Point out each Plasmodium parasite.
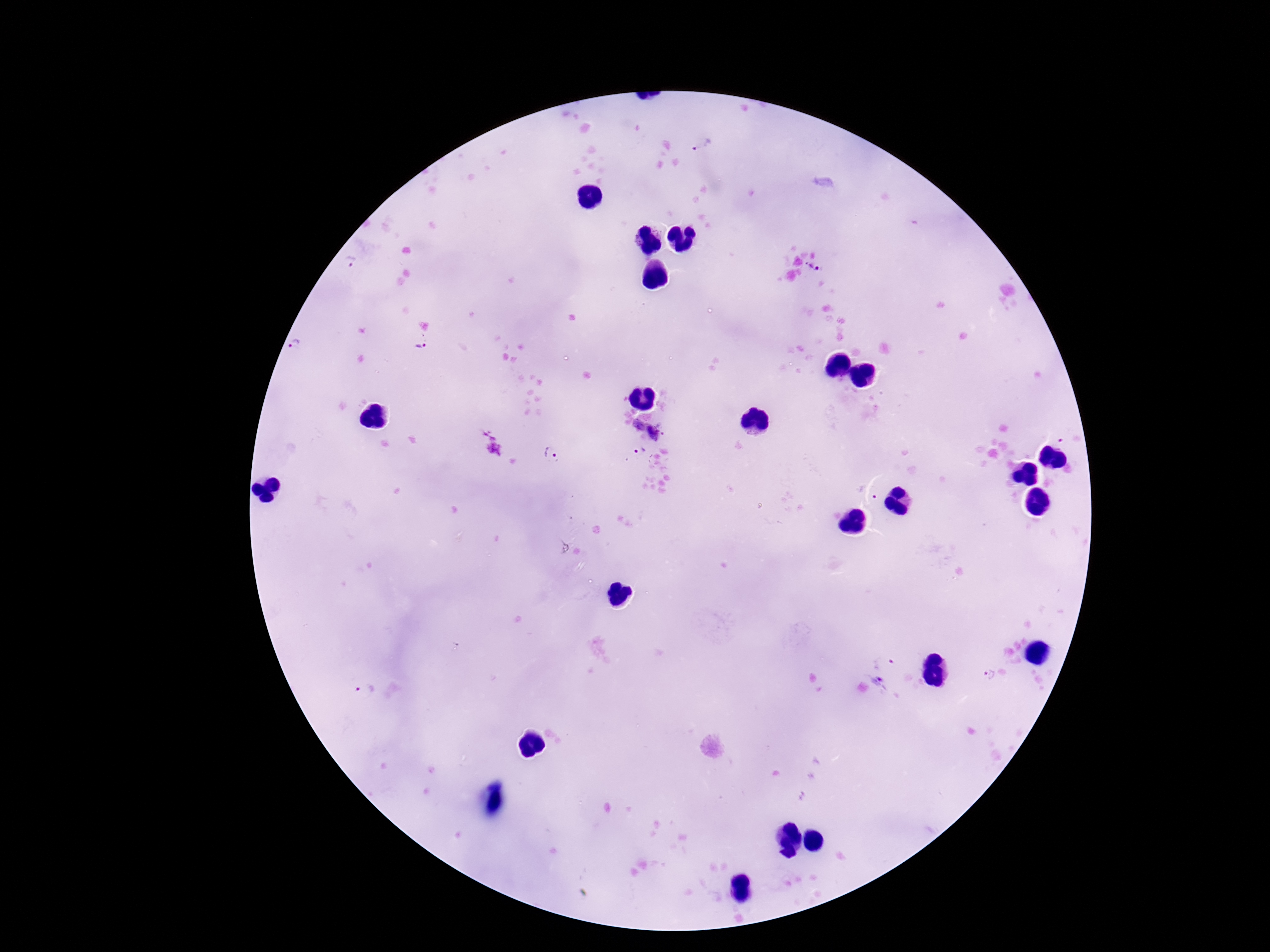
Approximate centers as [x, y] in pixels.
Plasmodium parasites: [703, 145], [350, 261], [809, 266], [817, 269], [296, 345], [419, 345], [637, 425], [655, 434], [1060, 444], [641, 452], [551, 455], [883, 658], [986, 674], [880, 679], [365, 689].

Photographed through the microscope eyepiece with a smartphone camera. 100x magnification. Thick blood smear. Giemsa-stained preparation. Single field of view. Image is 1270×952 pixels. Patient malaria status: positive.